Name the parasite shown.
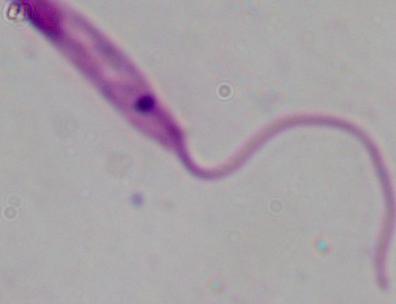

This is Leishmania.

Captured at 1000x magnification. Photomicrograph.